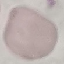

malaria status = uninfected
capture = smartphone camera at the microscope eyepiece
image type = cell patch, automatically extracted from a larger field of view and resized to 64 × 64 pixels
preparation = thin blood film
stain = Giemsa